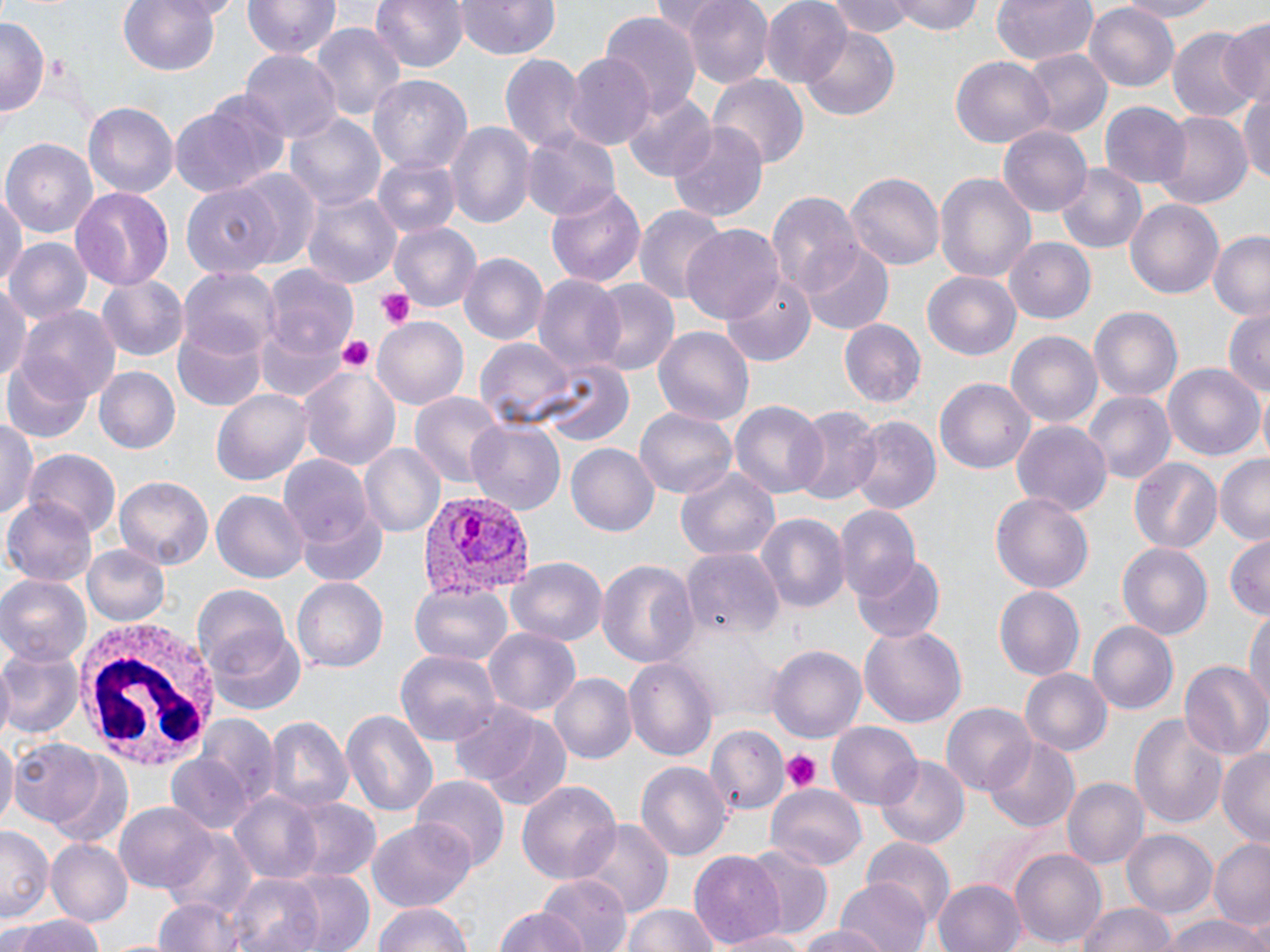
Approximate bounding boxes as [x1, y1, x2, y2] in pixels. Platelet locations: [377, 288, 416, 329], [337, 334, 376, 376], [781, 750, 820, 791]. Plasmodium vivax-infected red blood cell locations: [416, 488, 533, 602]. Uninfected red blood cell locations: [118, 0, 222, 77], [244, 0, 340, 60], [371, 0, 468, 74], [455, 0, 558, 60], [682, 0, 774, 88], [824, 0, 916, 39], [894, 0, 983, 35], [990, 0, 1098, 65], [1111, 0, 1227, 22], [760, 1, 851, 88], [1086, 1, 1179, 91], [600, 12, 701, 113], [1216, 16, 1270, 107], [0, 17, 46, 116], [311, 24, 405, 130], [1168, 24, 1259, 125], [799, 27, 898, 120], [1023, 48, 1111, 139], [239, 51, 340, 142], [500, 52, 587, 153], [564, 54, 656, 151], [951, 58, 1052, 147], [709, 74, 809, 168], [368, 75, 472, 176], [618, 90, 719, 182], [1239, 90, 1270, 189], [169, 99, 281, 200], [84, 103, 177, 198], [1100, 103, 1189, 191], [1152, 110, 1252, 209], [285, 111, 387, 212], [446, 122, 534, 227], [668, 122, 769, 223], [998, 126, 1093, 216], [518, 129, 620, 219], [3, 136, 98, 239], [373, 158, 462, 240], [1057, 166, 1146, 253], [234, 169, 322, 267], [843, 170, 946, 269], [932, 170, 1037, 284], [545, 181, 647, 290], [0, 183, 25, 298], [182, 184, 278, 278], [69, 185, 173, 292], [767, 190, 863, 297], [302, 191, 401, 289], [1124, 196, 1227, 301], [635, 204, 726, 306], [391, 222, 481, 311], [683, 225, 786, 324], [1208, 230, 1270, 322], [1005, 237, 1096, 325], [5, 238, 91, 326], [802, 243, 894, 333], [459, 254, 547, 346], [178, 266, 279, 360], [262, 267, 360, 363], [923, 271, 1022, 359], [722, 274, 815, 366], [98, 275, 187, 361], [533, 275, 627, 383], [587, 280, 683, 377], [0, 287, 31, 388], [1088, 306, 1183, 404], [20, 308, 121, 405], [1222, 309, 1269, 400], [254, 315, 351, 402], [373, 315, 469, 408], [174, 316, 265, 412], [837, 317, 925, 407], [655, 327, 752, 429], [1005, 329, 1102, 426], [474, 337, 575, 424], [4, 356, 94, 444], [540, 360, 631, 447], [1163, 360, 1264, 460], [299, 363, 402, 470], [93, 366, 179, 454], [935, 378, 1034, 473], [212, 388, 316, 486], [1086, 391, 1174, 485], [408, 392, 505, 488], [730, 402, 826, 497], [792, 405, 882, 506], [637, 407, 737, 500], [0, 415, 39, 523], [848, 417, 939, 515], [468, 419, 566, 515], [1011, 419, 1113, 517], [361, 442, 446, 537], [566, 443, 659, 537], [25, 451, 118, 538], [1214, 453, 1270, 543], [280, 457, 374, 548], [1127, 457, 1221, 554], [676, 464, 783, 567], [116, 478, 211, 569], [213, 490, 307, 584], [991, 492, 1093, 593], [3, 498, 97, 585], [836, 505, 922, 601], [295, 507, 388, 587], [754, 513, 848, 616], [1225, 535, 1269, 618], [1116, 542, 1212, 639], [83, 546, 168, 624], [683, 548, 785, 639], [852, 554, 944, 644], [597, 557, 698, 672], [506, 559, 607, 644], [0, 575, 90, 665], [292, 578, 388, 672], [411, 582, 514, 666], [993, 583, 1085, 679], [192, 586, 293, 675], [1245, 606, 1269, 711], [1088, 619, 1179, 713], [859, 625, 968, 730], [482, 627, 581, 720], [204, 628, 306, 717], [768, 644, 866, 745], [0, 648, 83, 741], [394, 649, 500, 748], [626, 654, 718, 764], [1179, 664, 1268, 762], [1021, 669, 1112, 756], [550, 673, 635, 765], [450, 700, 573, 810], [942, 704, 1037, 798], [340, 707, 437, 818], [1130, 711, 1227, 832], [263, 714, 353, 813], [201, 715, 277, 811], [829, 724, 923, 808], [707, 729, 787, 812], [0, 732, 16, 828], [9, 739, 105, 827], [983, 739, 1079, 831], [1218, 746, 1269, 847], [46, 752, 135, 849], [166, 754, 256, 837], [876, 757, 968, 850], [636, 763, 730, 859], [411, 776, 509, 869], [1062, 777, 1147, 869], [517, 781, 624, 887], [766, 785, 867, 869], [230, 792, 326, 884], [272, 797, 382, 884], [115, 802, 219, 893], [369, 819, 475, 915], [576, 820, 670, 919], [1121, 827, 1217, 919], [0, 829, 51, 924], [164, 832, 260, 925], [1210, 837, 1270, 929], [43, 838, 132, 927], [864, 839, 956, 930], [1011, 848, 1106, 950], [690, 849, 786, 951], [739, 849, 834, 940], [282, 868, 374, 952], [229, 873, 326, 952], [536, 874, 631, 952], [835, 877, 932, 952], [933, 879, 1026, 952], [148, 897, 253, 952], [373, 900, 474, 952], [1076, 901, 1177, 952], [622, 904, 723, 952], [494, 907, 587, 952], [3, 914, 110, 952], [1160, 914, 1270, 952], [794, 924, 892, 952], [719, 930, 820, 952]. White blood cell locations: [75, 614, 220, 766]. Slide-level diagnosis: Plasmodium vivax. Optical microscopy. Single field of view. May-Grünwald-Giemsa-stained preparation. Image is 1270×952 pixels. Thin blood smear. Captured at 1000x magnification.